Comment on the morphology of the red blood cells.
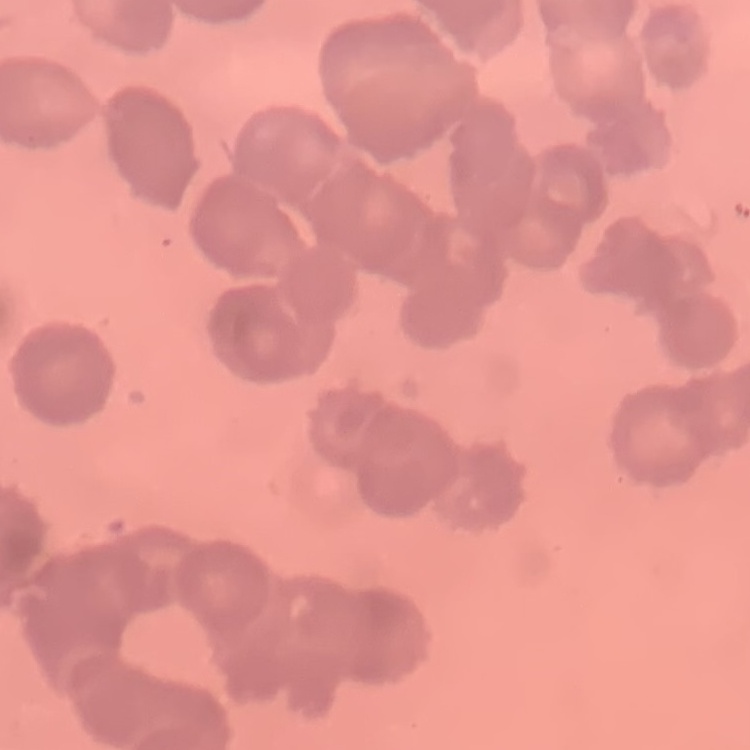

Rouleaux formation.

Summary:
  - Image type: square crop of a larger photomicrograph
  - Preparation: thin blood smear
  - Stain: Field's or Giemsa